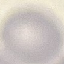
Malaria status: uninfected. Giemsa-stained preparation. Cell patch, automatically extracted from a larger field of view and resized to 64 × 64 pixels. Acquired by smartphone through the microscope eyepiece. Thin blood film.